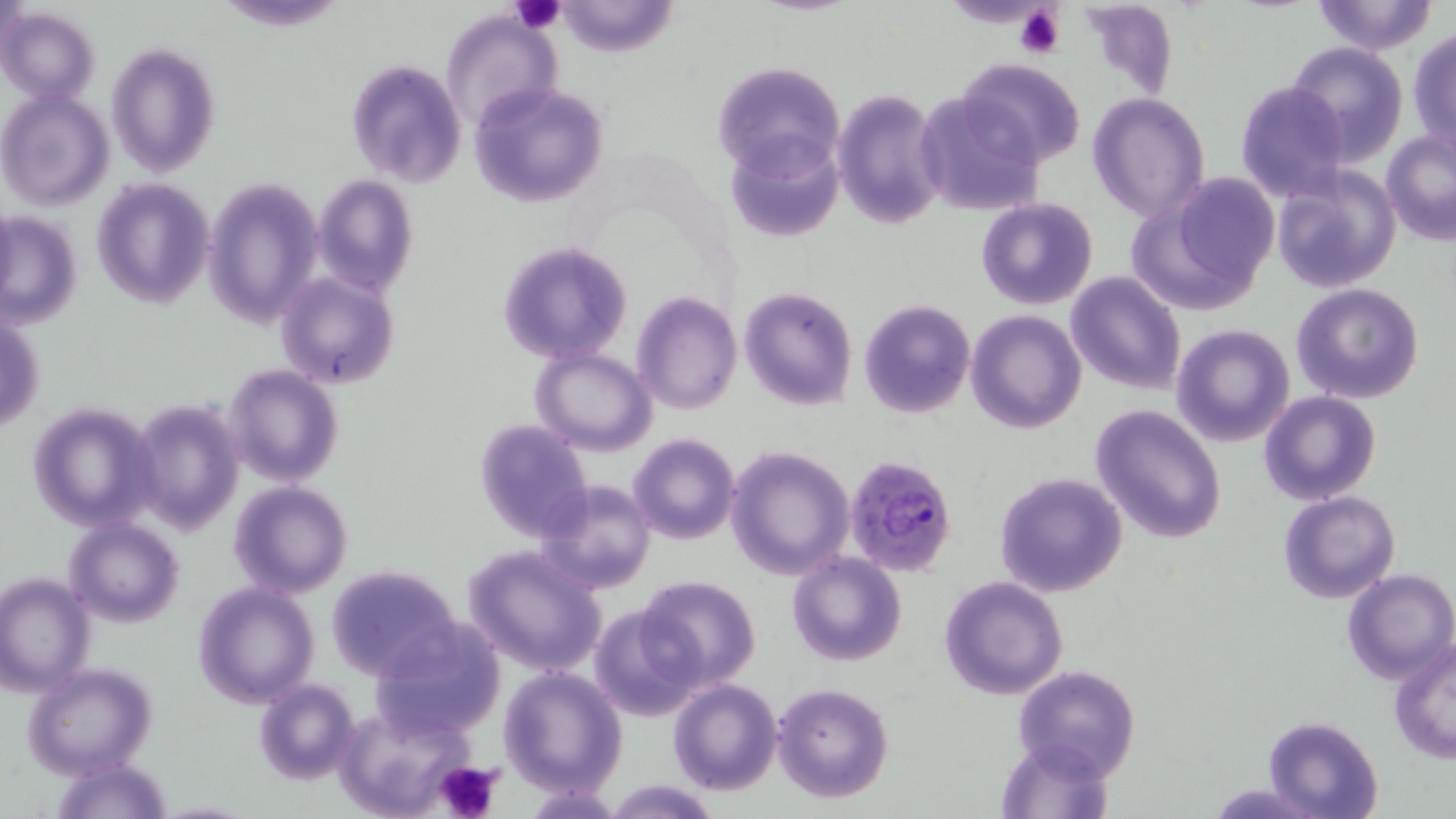
slide-level diagnosis = Plasmodium falciparum
field of view = single
uninfected red blood cell locations = approximate bounding boxes as (x1, y1, x2, y2) in pixels: (1312, 0, 1439, 55), (553, 1, 678, 57), (0, 8, 100, 106), (439, 9, 561, 132), (1409, 28, 1456, 152), (106, 42, 222, 179), (1286, 42, 1409, 166), (957, 58, 1086, 168), (345, 60, 466, 189), (713, 62, 845, 181), (1234, 81, 1352, 202), (469, 84, 610, 208), (913, 89, 1044, 218), (1, 90, 115, 211), (832, 90, 946, 231), (1088, 92, 1211, 221), (1381, 128, 1456, 247), (727, 133, 845, 243), (1271, 166, 1401, 294), (314, 174, 417, 297), (1133, 176, 1278, 310), (91, 178, 215, 310), (202, 178, 324, 329), (976, 197, 1097, 311), (1, 212, 82, 329), (498, 240, 632, 363), (1065, 270, 1187, 395), (276, 271, 399, 388), (1290, 282, 1425, 404), (739, 285, 857, 410), (632, 291, 741, 414), (860, 300, 976, 419), (966, 309, 1087, 433), (1, 310, 45, 433), (1170, 323, 1295, 448), (530, 346, 658, 455), (222, 363, 345, 486), (1259, 392, 1381, 507), (128, 398, 245, 535), (27, 402, 159, 532), (1090, 403, 1227, 544), (473, 418, 595, 542), (628, 433, 740, 544), (724, 445, 857, 580), (994, 471, 1128, 597), (534, 479, 656, 595), (228, 481, 353, 599), (1278, 490, 1401, 603), (62, 518, 184, 627), (462, 546, 608, 677), (786, 551, 907, 666), (324, 565, 466, 681), (1342, 568, 1456, 686), (0, 572, 95, 697), (636, 574, 762, 690), (939, 576, 1069, 699), (193, 582, 320, 709), (588, 604, 703, 723), (371, 619, 508, 740), (1389, 638, 1455, 765), (22, 662, 158, 780), (1012, 664, 1141, 781), (498, 665, 628, 797), (252, 678, 361, 786), (666, 678, 782, 796), (771, 682, 894, 804), (333, 703, 481, 818), (1262, 715, 1383, 819), (994, 736, 1115, 818), (49, 759, 174, 819), (605, 781, 722, 818), (1207, 781, 1318, 818)
preparation = thin blood smear
modality = light microscopy
stain = May-Grünwald-Giemsa
Plasmodium falciparum-infected red blood cell locations = approximate bounding boxes as (x1, y1, x2, y2) in pixels: (844, 453, 959, 576)
magnification = 1000x
platelet locations = approximate bounding boxes as (x1, y1, x2, y2) in pixels: (512, 0, 566, 35), (1015, 6, 1066, 59), (434, 759, 505, 819)
image size = 1456×819 pixels